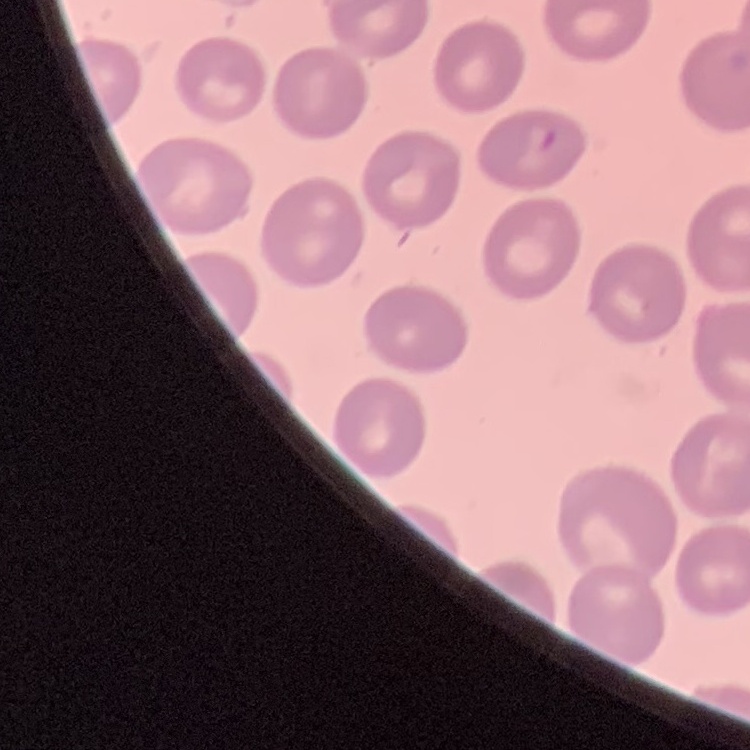 The red blood cells show no rouleaux formation. Field's or Giemsa stain. One tile cut from a larger photomicrograph. Thin peripheral smear.